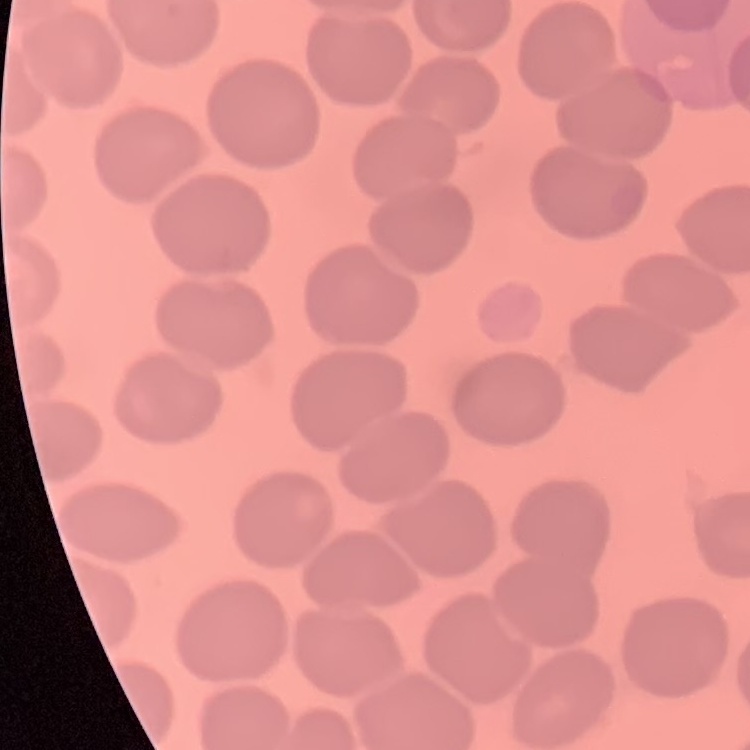 The erythrocytes show no rouleaux formation. Thin blood smear. Square crop of a larger photomicrograph. Stained with either Field's or Giemsa.